Locate and identify every blood parasite.
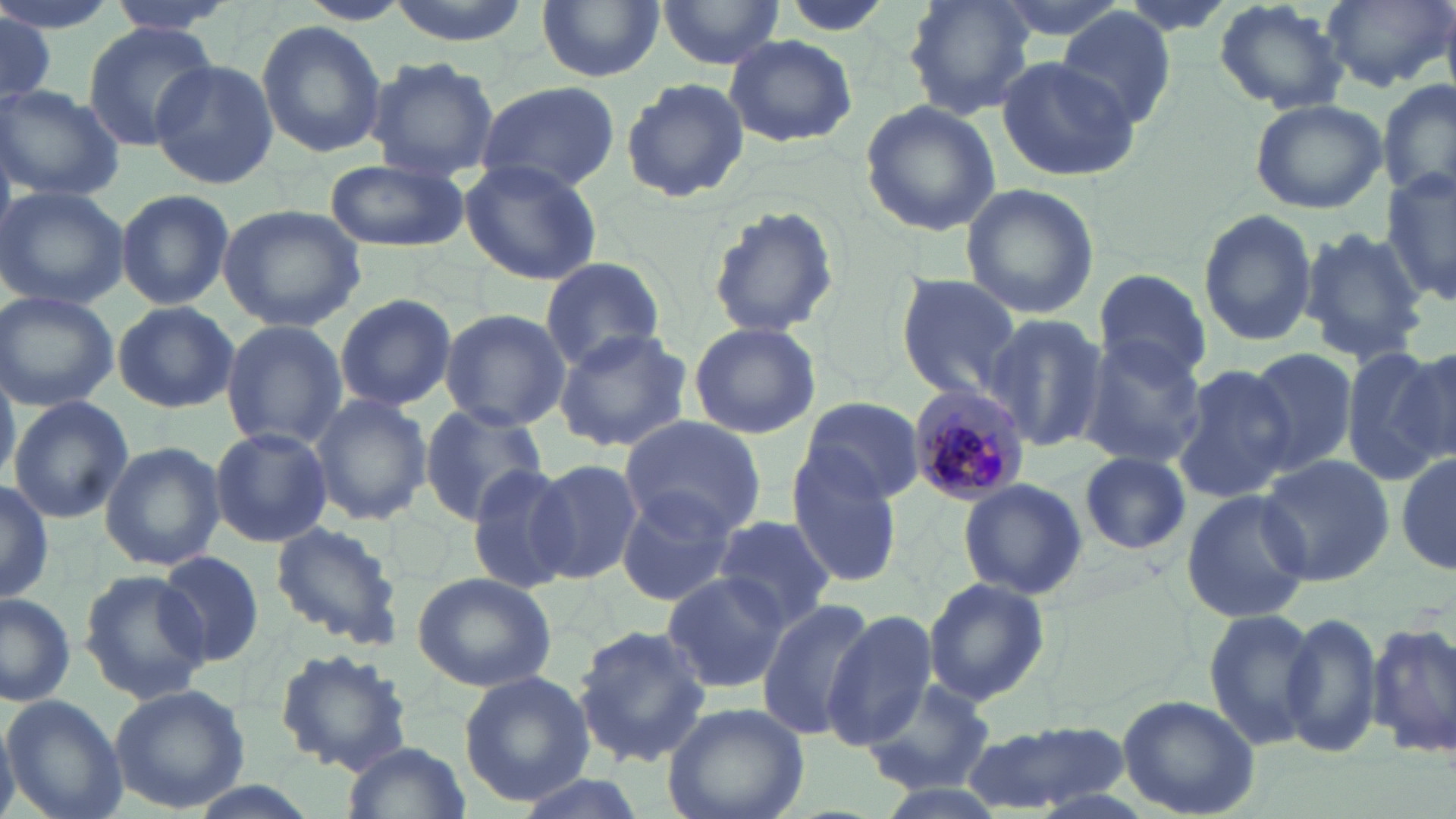
Approximate bounding boxes as [x1, y1, x2, y2] in pixels.
Plasmodium malariae-infected red blood cells: [908, 381, 1034, 504].
No Plasmodium falciparum, Plasmodium ovale, Plasmodium vivax, Babesia divergens, or Trypanosoma brucei observed.

Summary:
  - Uninfected red blood cell locations: [105, 0, 240, 35], [382, 0, 534, 45], [535, 0, 665, 83], [904, 0, 1037, 119], [985, 0, 1140, 43], [1212, 0, 1348, 113], [1321, 0, 1453, 92], [295, 1, 413, 27], [657, 1, 781, 71], [0, 7, 58, 109], [1057, 8, 1175, 129], [256, 20, 387, 157], [81, 23, 218, 149], [725, 33, 857, 148], [364, 56, 499, 181], [997, 56, 1139, 180], [150, 57, 279, 188], [620, 78, 750, 204], [1379, 78, 1456, 206], [474, 80, 622, 195], [0, 85, 125, 201], [1249, 98, 1388, 213], [860, 99, 1000, 236], [324, 159, 468, 252], [459, 159, 604, 285], [1380, 167, 1455, 310], [959, 183, 1100, 321], [0, 185, 129, 311], [114, 189, 234, 310], [218, 204, 368, 330], [704, 204, 842, 338], [1201, 205, 1320, 346], [1297, 226, 1426, 362], [540, 257, 667, 372], [1092, 268, 1212, 386], [894, 273, 1024, 400], [0, 291, 119, 411], [333, 293, 457, 411], [112, 301, 238, 413], [437, 307, 569, 430], [981, 314, 1108, 453], [220, 319, 348, 451], [688, 321, 820, 440], [553, 329, 693, 453], [1081, 335, 1208, 467], [1394, 344, 1456, 463], [1346, 346, 1450, 482], [1243, 348, 1355, 474], [1170, 365, 1294, 504], [0, 367, 19, 488], [309, 393, 434, 524], [7, 394, 133, 523], [801, 396, 922, 502], [417, 404, 548, 525], [620, 416, 768, 538], [210, 425, 333, 546], [100, 441, 225, 573], [1078, 452, 1191, 556], [1396, 453, 1456, 576], [1259, 455, 1393, 585], [788, 456, 905, 587], [528, 457, 642, 584], [463, 461, 580, 594], [957, 479, 1088, 601], [0, 480, 55, 604], [613, 486, 743, 607], [1179, 488, 1312, 624], [712, 515, 840, 631], [269, 521, 405, 649], [156, 551, 264, 668], [79, 568, 212, 702], [410, 571, 557, 692], [659, 572, 790, 695], [922, 575, 1050, 705], [0, 593, 76, 707], [755, 598, 880, 739], [1203, 609, 1320, 749], [1279, 610, 1384, 759], [822, 611, 938, 747], [1369, 619, 1456, 758], [573, 624, 713, 765], [273, 649, 413, 778], [459, 671, 595, 805], [862, 680, 997, 796], [108, 683, 251, 813], [1, 694, 127, 819], [1117, 694, 1261, 818], [661, 700, 810, 819], [0, 711, 21, 819], [962, 724, 1129, 814], [340, 740, 472, 819], [506, 770, 653, 819]
  - Slide-level diagnosis: Plasmodium malariae
  - Stain: May-Grünwald-Giemsa
  - Image size: 1456×819 pixels
  - Modality: optical microscopy
  - Preparation: thin blood film
  - Magnification: 1000x
  - Field of view: single